Classify this cell by malaria status.
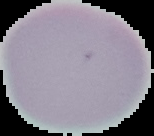
It is uninfected.

From a thin blood smear. Cell region segmented out of the field of view; the surrounding area is masked to black. Image is 154×136 pixels.